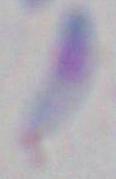 Toxoplasma gondii is seen. Photomicrograph. 1000x magnification.